Assess this cell for malaria.
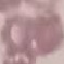
It is uninfected.

Summary:
  - Preparation: thin blood film
  - Stain: Giemsa
  - Capture: smartphone through the microscope eyepiece
  - Image type: automatically extracted cell patch, resized to 64 × 64 pixels